Assess this cell for malaria.
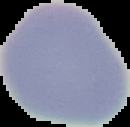
It is uninfected.

Image is 130×127 pixels. The area outside the segmented cell region is set to black. From a thin blood film.